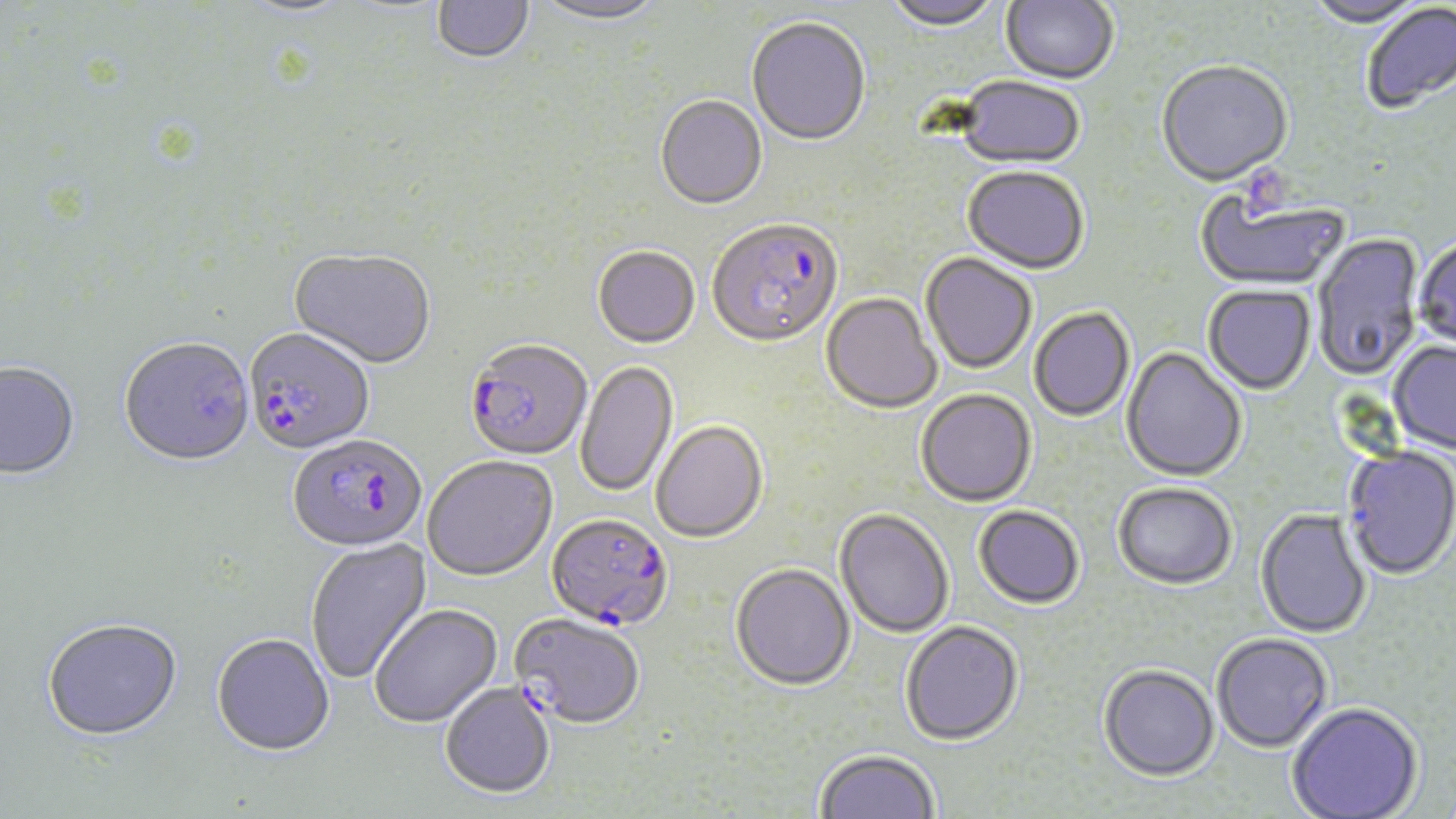

slide-level diagnosis = Plasmodium falciparum
stain = May-Grünwald-Giemsa
image size = 1456×819 pixels
magnification = 1000x
uninfected red blood cell locations = approximate bounding boxes as (x1,y1)-(x2,y2) corner pairs in pixels: (530,0)-(670,28), (882,0)-(1003,34), (1000,0)-(1118,87), (1304,0)-(1427,30), (235,1)-(356,20), (432,1)-(535,66), (1361,3)-(1456,116), (746,19)-(871,148), (1156,62)-(1293,189), (954,77)-(1085,172), (655,97)-(767,212), (961,168)-(1088,276), (1196,193)-(1348,291), (1313,233)-(1424,383), (1413,238)-(1456,354), (593,248)-(700,350), (289,250)-(435,371), (920,253)-(1037,376), (1203,286)-(1316,396), (821,293)-(942,415), (1029,308)-(1135,422), (119,339)-(256,469), (1389,342)-(1456,455), (1120,347)-(1247,483), (576,361)-(678,498), (0,363)-(80,482), (915,391)-(1037,509), (651,422)-(768,545), (1341,448)-(1456,582), (423,457)-(558,583), (1113,484)-(1236,592), (973,507)-(1084,611), (1255,509)-(1371,640), (835,510)-(954,639), (305,538)-(433,684), (730,565)-(855,693), (370,605)-(504,730), (43,620)-(183,744), (900,623)-(1024,747), (1211,634)-(1334,754), (212,636)-(335,759), (1098,666)-(1219,784), (441,684)-(555,800), (1287,704)-(1423,819), (815,749)-(940,818)
field of view = one of a larger specimen
platelet locations = approximate bounding boxes as (x1,y1)-(x2,y2) corner pairs in pixels: (1243,164)-(1314,220)
preparation = thin blood film
modality = light microscopy
Plasmodium falciparum-infected red blood cell locations = approximate bounding boxes as (x1,y1)-(x2,y2) corner pairs in pixels: (708,222)-(843,352), (244,330)-(375,457), (465,342)-(592,464), (287,435)-(427,555), (546,516)-(673,634), (510,616)-(644,732)